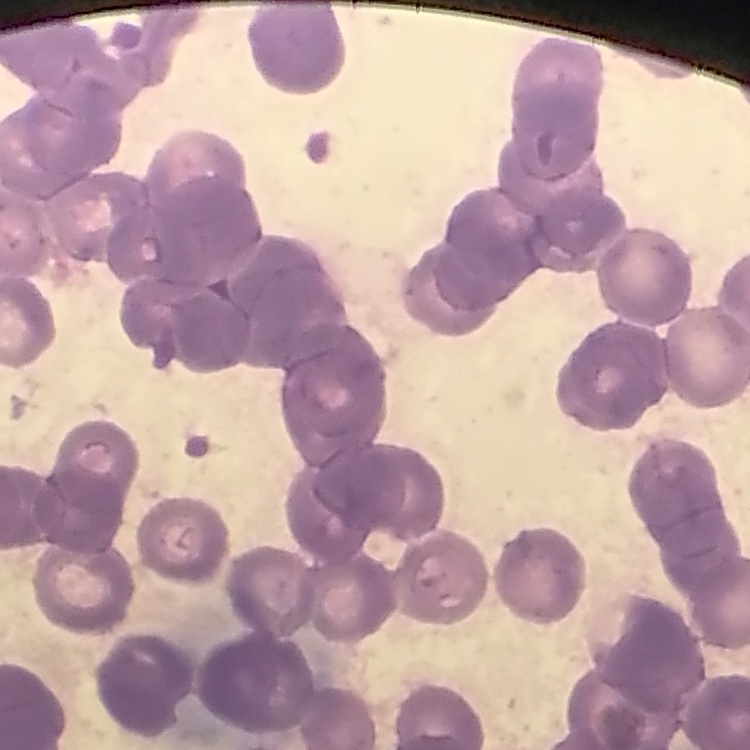

red blood cell morphology = rouleaux formation
preparation = thin blood smear
image type = one tile cut from a larger photomicrograph
stain = Field's or Giemsa